Name the cell type shown.
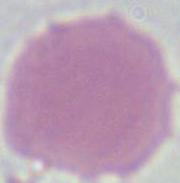
This is an erythrocyte.

{
  "magnification": "1000x",
  "modality": "photomicrograph"
}